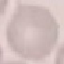

Malaria status: uninfected. Giemsa stain. Thin blood smear. Photographed with a smartphone camera at the microscope eyepiece. Cell patch, automatically extracted from a larger field of view and resized to 64 × 64 pixels.